Report the malaria status.
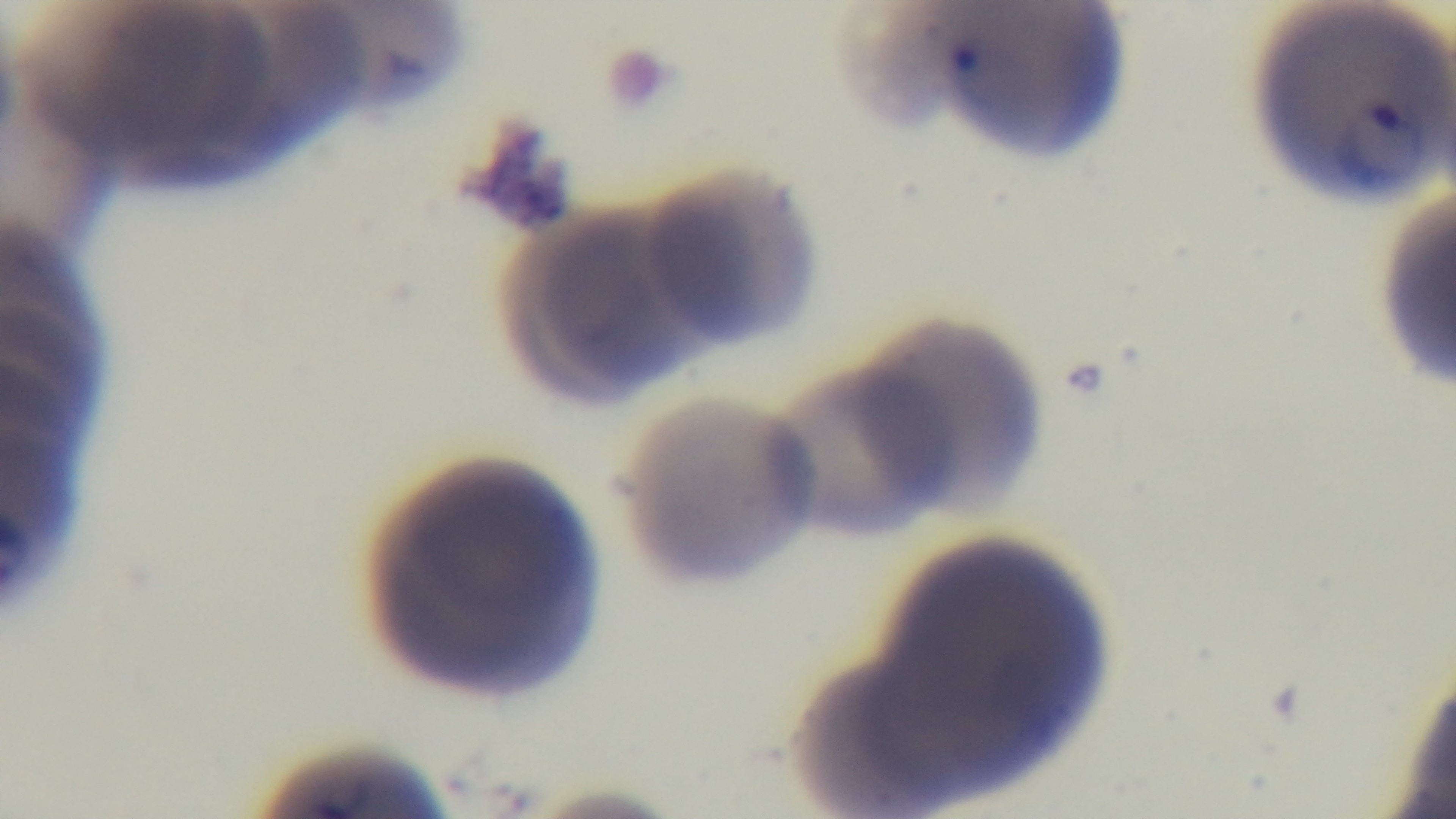

It is infected.

{
  "field_of_view": "one from the slide",
  "modality": "light microscopy",
  "preparation": "thin blood film",
  "stain": "Giemsa",
  "capture": "mounted 4K digital camera",
  "objective": "100x oil immersion"
}